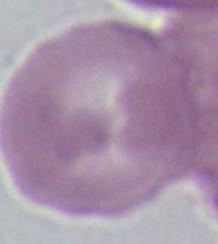
modality = micrograph
identification = erythrocyte
magnification = 1000x